Report the malaria status of this cell.
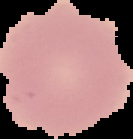

It is uninfected.

image_size: 133×139 pixels
image_type: cell region segmented out of the field of view; surrounding area masked to black
preparation: thin blood film